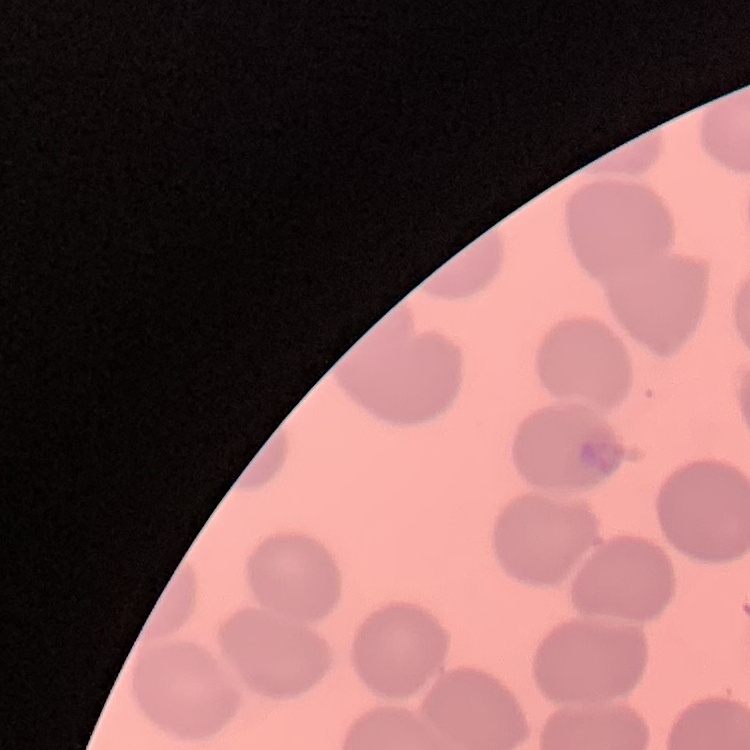
Summary:
  - Red blood cell morphology: no rouleaux formation
  - Preparation: thin peripheral smear
  - Stain: Field's or Giemsa
  - Image type: one tile cut from a larger photomicrograph